Locate every blood parasite and identify its species.
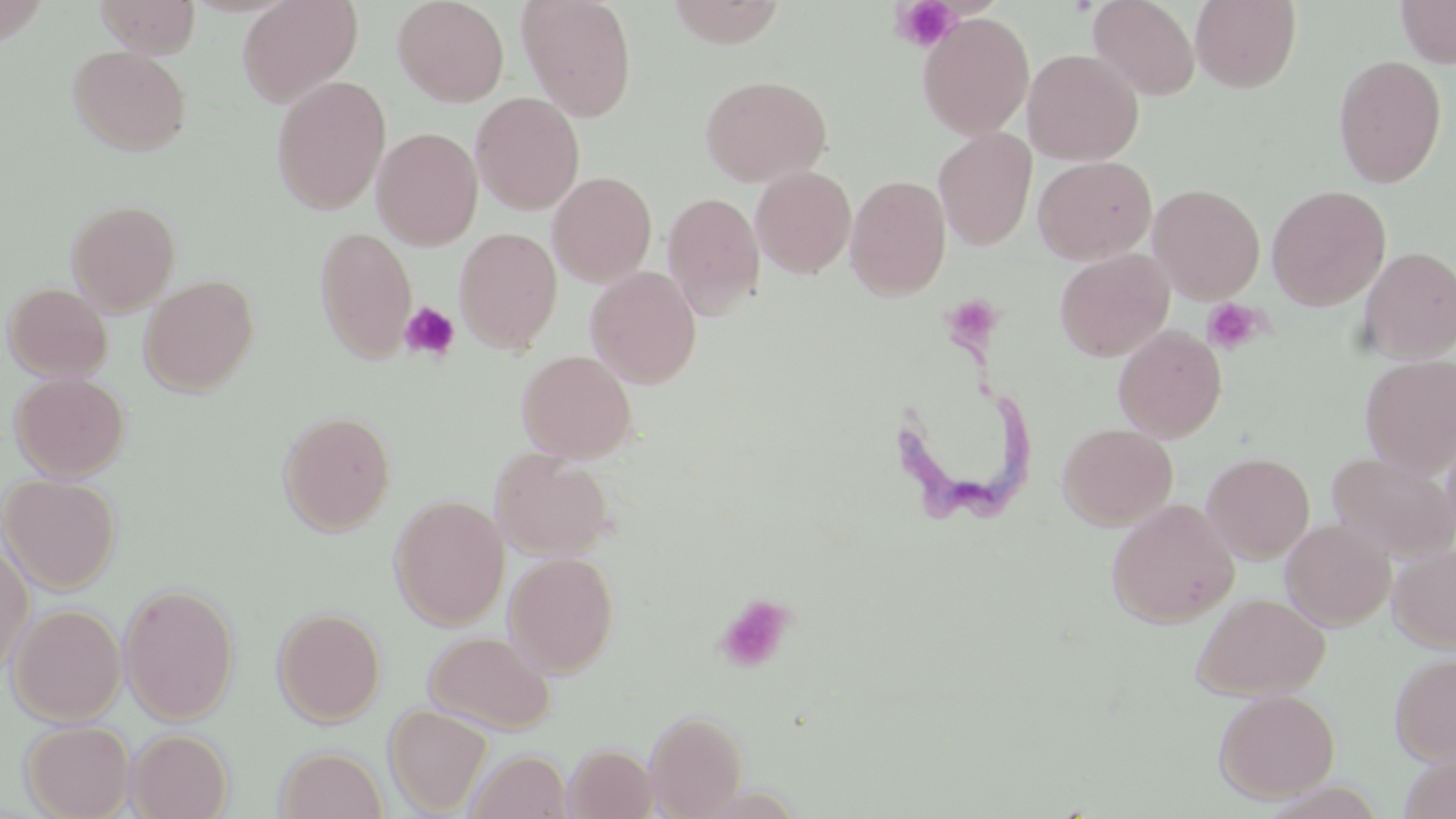
Approximate bounding boxes as (x1,y1)-(x2,y2) corner pairs in pixels.
Trypanosoma brucei: (879,330)-(1032,540).
No Plasmodium falciparum, Plasmodium ovale, Plasmodium malariae, Plasmodium vivax, or Babesia divergens observed.

Platelet locations: (890,0)-(961,53), (956,299)-(1007,349), (1202,299)-(1265,354), (399,300)-(460,362), (713,593)-(796,674). Uninfected red blood cell locations: (94,0)-(201,57), (237,0)-(363,107), (392,0)-(510,107), (516,0)-(638,122), (666,0)-(786,47), (1088,0)-(1200,101), (1190,0)-(1302,92), (1394,0)-(1456,68), (917,12)-(1035,140), (68,44)-(191,156), (1023,48)-(1144,165), (1332,54)-(1447,188), (699,74)-(831,187), (270,75)-(391,214), (470,92)-(585,215), (371,126)-(484,249), (933,128)-(1037,250), (1033,155)-(1156,264), (751,166)-(856,279), (548,170)-(657,287), (845,174)-(951,300), (1148,183)-(1265,303), (1267,185)-(1391,310), (662,191)-(765,319), (65,198)-(181,314), (314,226)-(418,363), (454,227)-(563,354), (1358,246)-(1456,362), (1054,249)-(1175,363), (585,265)-(702,388), (140,274)-(259,396), (2,281)-(113,381), (1113,325)-(1227,442), (516,349)-(637,463), (1359,354)-(1456,477), (9,371)-(130,481), (277,410)-(396,536), (1058,423)-(1178,530), (1440,428)-(1456,555), (491,448)-(615,560), (1327,451)-(1456,561), (1202,452)-(1315,562), (1,473)-(121,593), (389,494)-(510,629), (1107,499)-(1239,628), (1281,518)-(1395,630), (0,542)-(34,680), (1388,542)-(1456,653), (504,551)-(619,677), (118,582)-(239,724), (1192,591)-(1331,700), (8,603)-(126,725), (274,607)-(386,726), (424,630)-(556,735), (1390,651)-(1456,765), (1213,688)-(1340,803), (384,704)-(492,816), (645,709)-(748,819), (20,719)-(135,818), (127,729)-(233,819), (565,744)-(658,819), (275,746)-(388,819), (466,749)-(571,819), (1399,754)-(1455,818). Slide-level diagnosis: Trypanosoma brucei. May-Grünwald-Giemsa-stained preparation. Image is 1456×819 pixels. Thin blood smear. Optical microscopy. Captured at 1000x magnification. Single field of view.